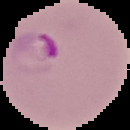
Segmented cell region on a black background. Image is 130×130 pixels. Result: Plasmodium parasites detected. From a thin blood film.